Comment on the morphology of the red blood cells.
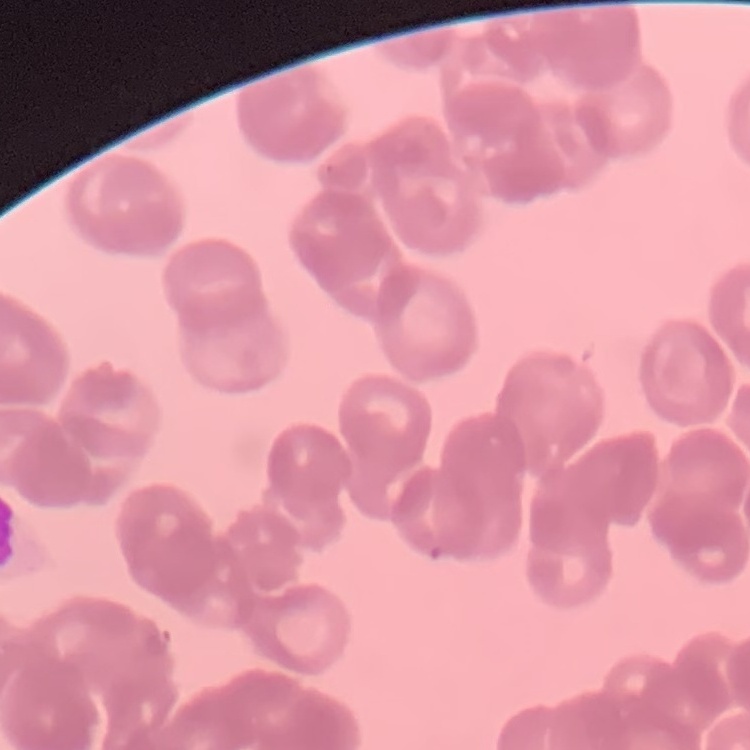
They show rouleaux formation.

Summary:
  - Image type: one tile cut from a larger photomicrograph
  - Preparation: thin blood film
  - Stain: Field's or Giemsa